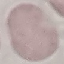
Malaria status: uninfected. Thin blood smear. Giemsa stain. Photographed with a smartphone camera at the microscope eyepiece. Automatically extracted cell patch, resized to 64 × 64 pixels.